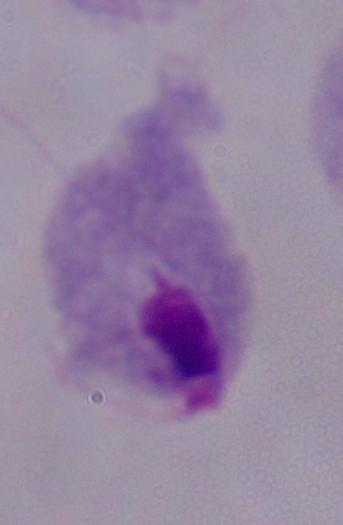
A trichomonad is shown. Micrograph. Captured at 1000x magnification.